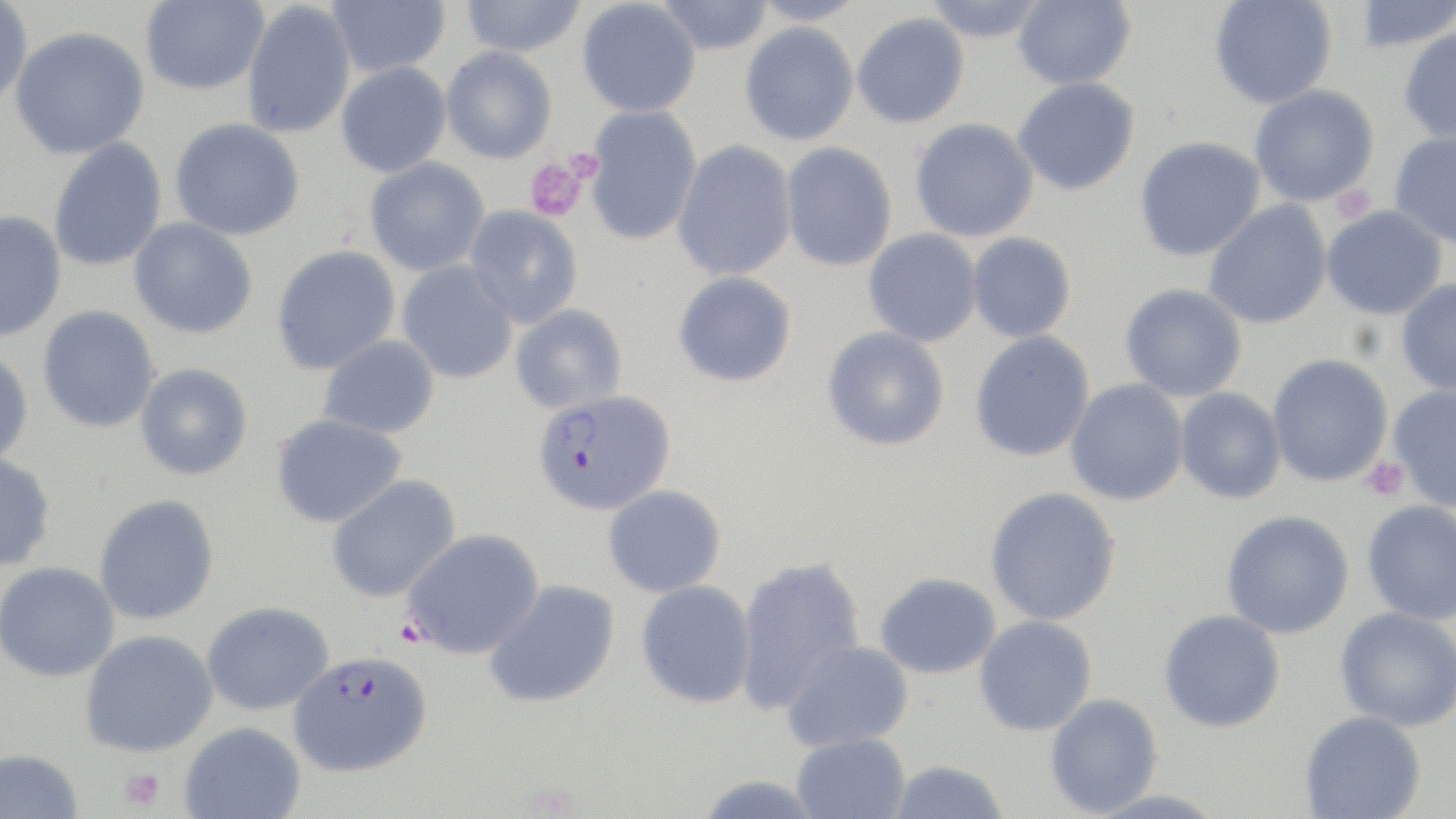
Summary:
  - Coordinate format: approximate bounding boxes as (x1,y1)-(x2,y2) corner pairs in pixels
  - Uninfected red blood cell locations: (0,0)-(33,107), (140,0)-(269,95), (327,0)-(450,78), (460,0)-(587,57), (577,0)-(701,118), (654,0)-(774,55), (748,0)-(866,26), (922,0)-(1050,43), (1013,0)-(1136,90), (1209,0)-(1337,109), (1353,0)-(1455,53), (241,1)-(356,138), (852,12)-(970,129), (739,22)-(859,146), (9,26)-(150,160), (1398,26)-(1456,143), (441,46)-(558,164), (336,62)-(451,178), (1012,77)-(1140,195), (1250,84)-(1379,207), (583,106)-(703,246), (169,118)-(305,241), (910,118)-(1039,242), (1389,130)-(1456,247), (1134,137)-(1265,262), (48,138)-(167,272), (672,140)-(797,282), (780,142)-(897,271), (364,157)-(490,277), (1203,201)-(1333,330), (464,205)-(583,328), (1321,206)-(1447,321), (0,210)-(67,343), (129,217)-(258,339), (863,228)-(982,347), (967,232)-(1077,343), (270,245)-(401,375), (397,261)-(518,384), (673,271)-(797,387), (1396,279)-(1456,395), (1119,283)-(1248,401), (511,304)-(627,414), (37,306)-(161,433), (822,326)-(950,451), (969,331)-(1095,462), (317,335)-(441,439), (0,348)-(34,467), (1267,354)-(1393,487), (134,363)-(253,480), (1065,378)-(1189,506), (1387,385)-(1456,512), (1175,387)-(1286,504), (270,413)-(408,528), (0,452)-(57,572), (325,474)-(462,603), (603,484)-(727,598), (984,487)-(1121,626), (93,494)-(220,626), (1361,500)-(1456,625), (1221,510)-(1355,639), (401,528)-(545,660), (734,554)-(867,715), (0,561)-(120,682), (875,572)-(1001,679), (483,579)-(621,708), (636,580)-(756,708), (201,602)-(334,715), (1335,607)-(1456,732), (1159,610)-(1286,733), (974,615)-(1097,736), (80,629)-(218,757), (781,640)-(914,752), (1044,693)-(1163,816), (1299,710)-(1426,818), (179,721)-(306,819), (791,732)-(910,819), (0,748)-(84,819), (885,760)-(1010,819), (694,774)-(827,818)
  - Platelet locations: (561,146)-(604,188), (524,156)-(590,221), (1329,185)-(1377,222), (1360,457)-(1410,502), (120,767)-(164,812)
  - Plasmodium falciparum-infected red blood cell locations: (532,389)-(676,515), (288,651)-(432,778)
  - Slide-level diagnosis: Plasmodium falciparum
  - Modality: optical microscopy
  - Stain: May-Grünwald-Giemsa
  - Field of view: single
  - Image size: 1456×819 pixels
  - Magnification: 1000x
  - Preparation: thin blood film